Assess this cell for malaria.
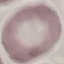
Uninfected.

Giemsa stain. Cell patch, automatically extracted from a larger field of view and resized to 64 × 64 pixels. Acquired by smartphone through the microscope eyepiece. Thin smear of blood.